Locate every leukocyte (white blood cell).
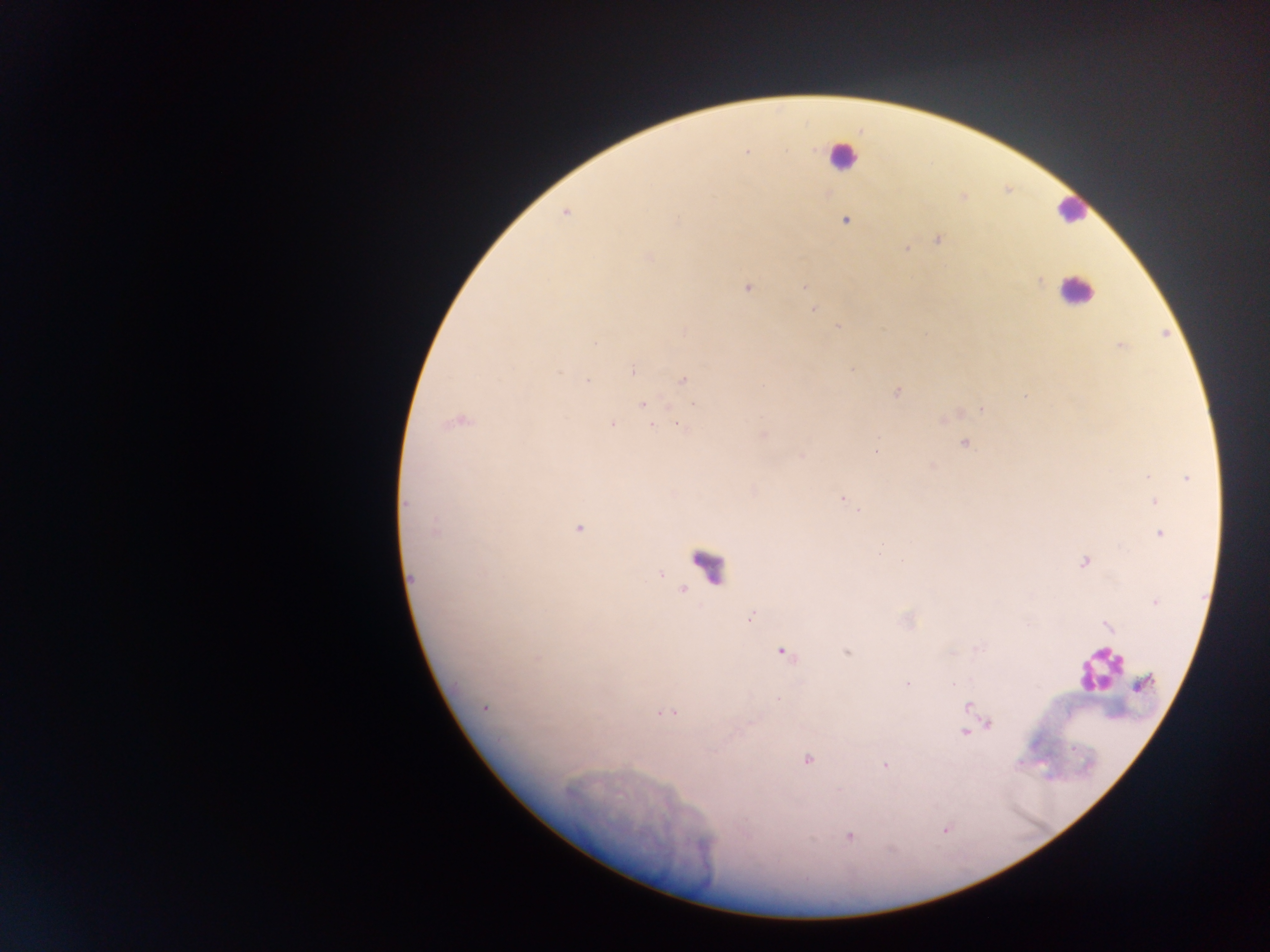

Approximate centers as [x, y] in pixels.
Leukocytes: [842, 155], [1071, 210], [1076, 290], [707, 564], [1097, 670].

Malaria parasite locations: [746, 151], [566, 213], [845, 220], [676, 222], [938, 239], [907, 248], [648, 257], [1040, 281], [805, 286], [748, 288], [812, 309], [837, 326], [596, 342], [1121, 347], [633, 371], [559, 372], [683, 380], [588, 381], [897, 392], [642, 404], [694, 404], [981, 409], [458, 421], [611, 424], [652, 425], [681, 426], [763, 435], [964, 443], [875, 452], [802, 456], [1147, 477], [1186, 478], [842, 499], [1153, 501], [406, 503], [859, 511], [578, 528], [434, 529], [1161, 534], [880, 554], [1083, 562], [661, 574], [412, 579], [1155, 602], [751, 617], [1107, 626], [783, 652], [847, 652], [907, 684], [777, 699], [969, 706], [485, 707], [665, 713], [989, 724], [964, 732], [807, 759], [885, 765], [850, 835]. Thick blood smear. Collected in Ghana. Image is 1270×952 pixels. Mobile-phone photograph taken through the microscope. Single field of view.